Give the extent of the Plasmodium falciparum parasites you find, grouped by life-cycle stage — ring form, trophozoite, schizont, or gametocyte.
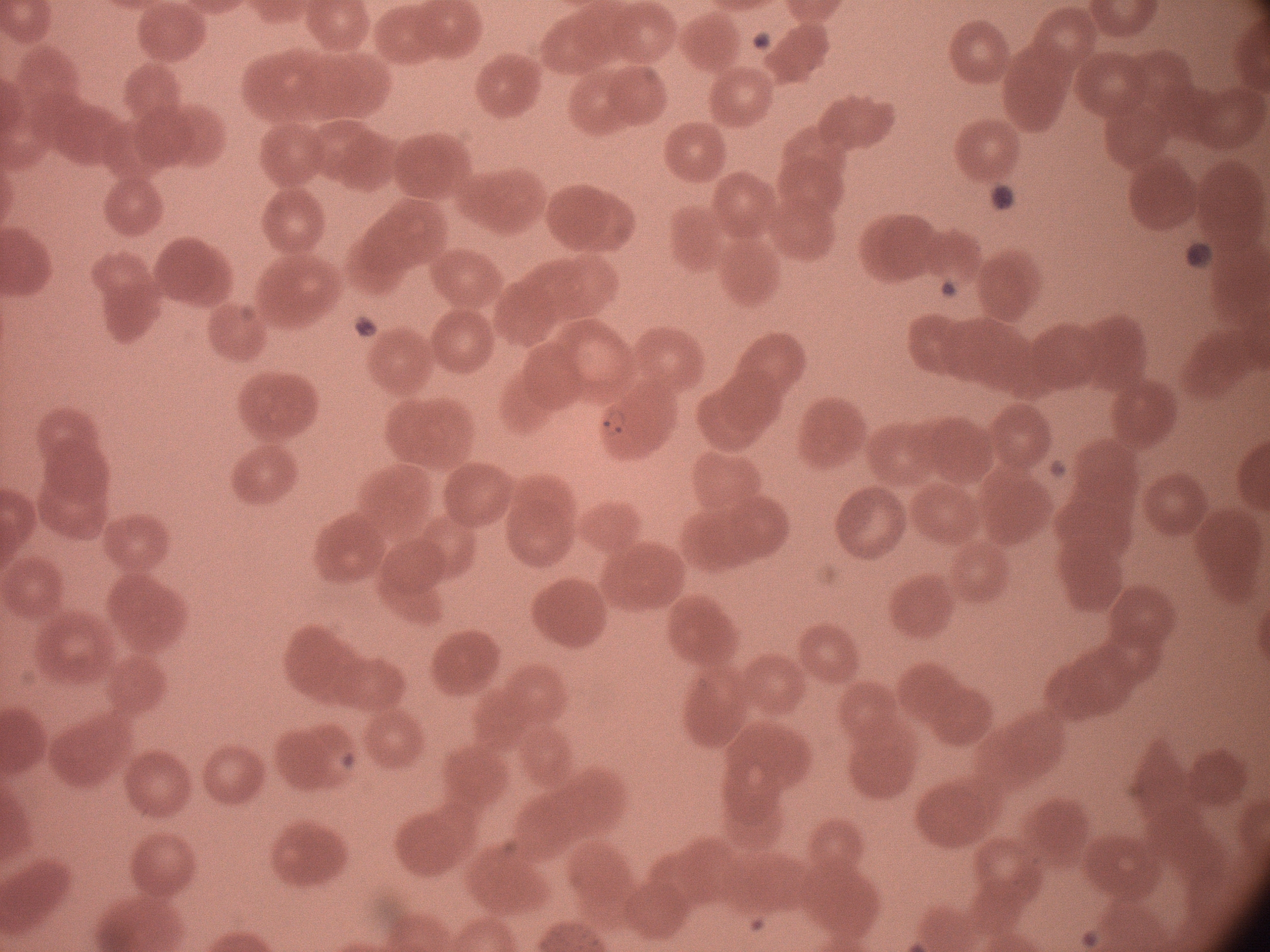
Approximate bounding boxes as (x1, y1, x2, y2) in pixels, from the source annotation, which is not necessarily exhaustive.
Ring forms: (595, 406, 631, 442).

Summary:
  - Microscope: Leica DM2000 with built-in camera
  - Preparation: thin blood smear
  - Image size: 1270×952 pixels
  - Field of view: one from this slide
  - Magnification: 100x
  - Stain: Giemsa
  - Species: Plasmodium falciparum